Describe the morphology of the erythrocytes.
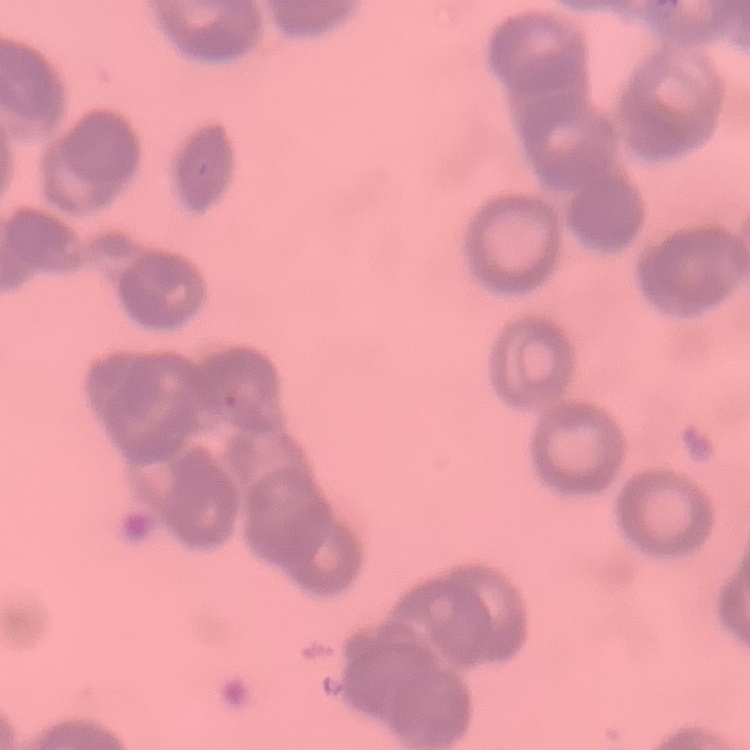
They show rouleaux formation.

stain = Field's or Giemsa
image type = square crop of a larger photomicrograph
preparation = thin blood smear